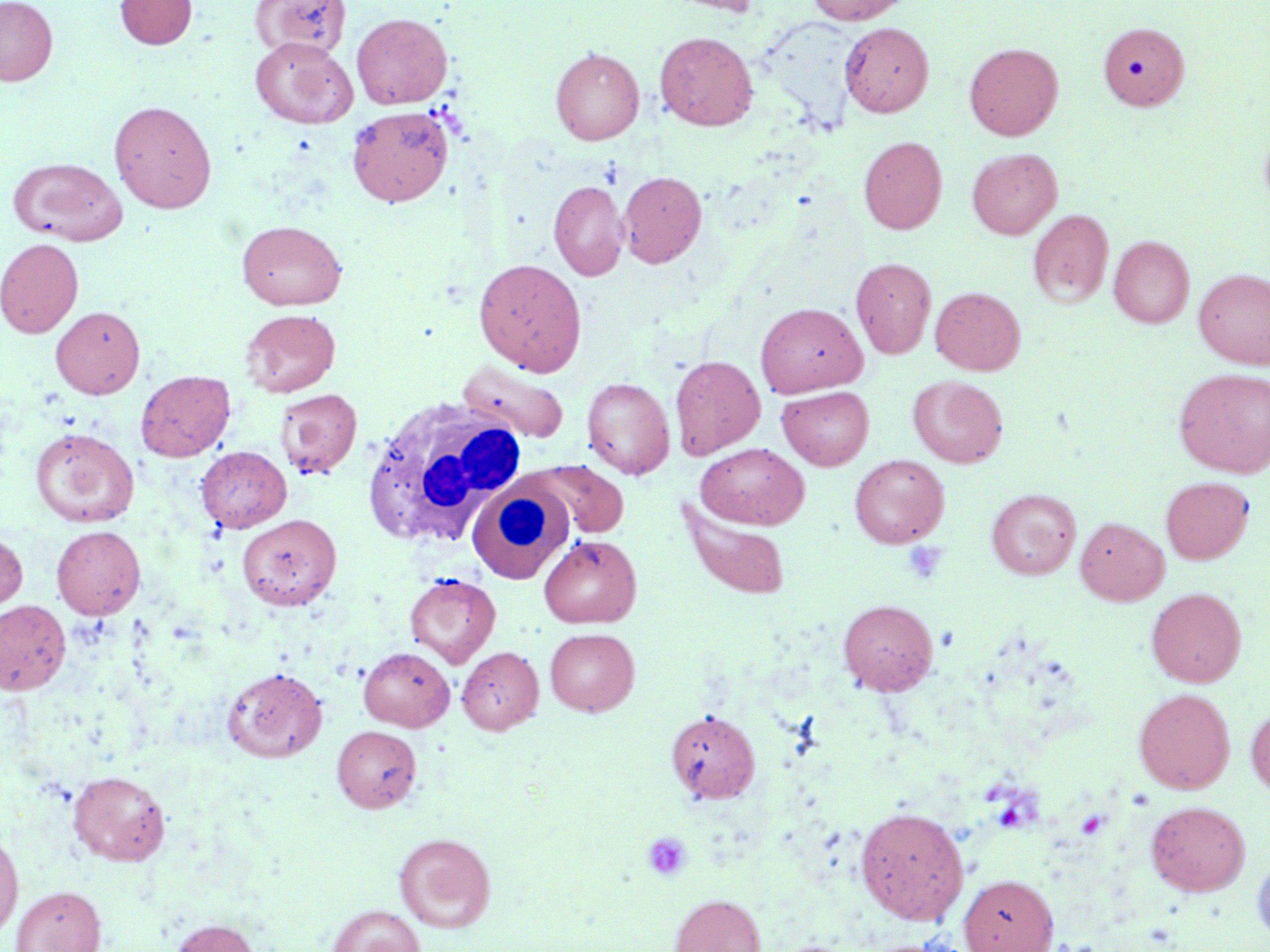

Summary:
  - Coordinate format: approximate bounding boxes as (x1,y1)-(x2,y2) corner pairs in pixels
  - White blood cell locations: (360,396)-(528,548), (466,481)-(574,584)
  - Platelet locations: (903,541)-(948,585), (642,831)-(692,882)
  - Uninfected red blood cell locations: (0,0)-(57,86), (115,0)-(197,49), (252,0)-(351,59), (665,0)-(762,15), (805,0)-(912,24), (351,12)-(452,109), (840,22)-(934,117), (1098,22)-(1189,110), (654,31)-(758,130), (250,36)-(357,128), (963,42)-(1063,140), (550,47)-(644,144), (109,99)-(217,213), (347,106)-(453,207), (1259,121)-(1270,218), (859,136)-(947,234), (966,147)-(1062,239), (8,157)-(128,245), (617,171)-(706,268), (548,180)-(628,280), (1027,209)-(1114,307), (236,220)-(347,310), (1109,236)-(1194,327), (0,238)-(83,337), (850,257)-(937,358), (473,258)-(587,375), (1194,268)-(1270,368), (930,286)-(1026,375), (755,302)-(868,396), (51,306)-(145,398), (240,308)-(340,397), (670,354)-(765,458), (457,360)-(570,444), (1174,368)-(1270,478), (136,370)-(235,461), (908,375)-(1008,468), (582,377)-(674,479), (776,386)-(874,470), (275,388)-(362,479), (30,427)-(139,527), (695,443)-(809,529), (196,446)-(291,532), (850,454)-(949,548), (529,460)-(629,539), (1160,476)-(1253,564), (986,489)-(1081,579), (678,503)-(791,600), (237,513)-(341,610), (1075,516)-(1169,605), (51,525)-(145,619), (0,530)-(28,616), (539,535)-(642,627), (405,572)-(501,667), (1146,587)-(1246,687), (838,599)-(937,695), (0,600)-(71,695), (545,627)-(639,715), (456,643)-(640,729), (456,646)-(543,734), (358,647)-(455,730), (222,666)-(327,762), (1134,688)-(1235,794), (1246,704)-(1270,797), (665,709)-(761,803), (331,725)-(422,812), (68,770)-(170,865), (1146,800)-(1250,896), (855,806)-(969,924), (0,829)-(23,941), (394,832)-(497,932), (1252,853)-(1270,948), (959,874)-(1058,952), (11,885)-(107,952), (668,894)-(766,952), (327,905)-(424,952), (169,918)-(261,952)
  - Slide-level diagnosis: negative for blood parasites
  - Modality: light microscopy
  - Stain: May-Grünwald-Giemsa
  - Magnification: 1000x
  - Field of view: one of a larger specimen
  - Image size: 1270×952 pixels
  - Preparation: thin blood smear